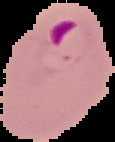
Summary:
  - Image size: 115×142 pixels
  - Preparation: thin blood film
  - Result: Plasmodium parasites detected
  - Image type: segmented cell region with the area outside set to black